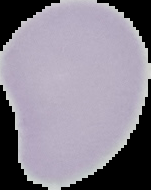

{
  "result": "negative for malaria parasites",
  "image_size": "151×190 pixels",
  "preparation": "thin blood smear",
  "image_type": "segmented cell region with the area outside set to black"
}